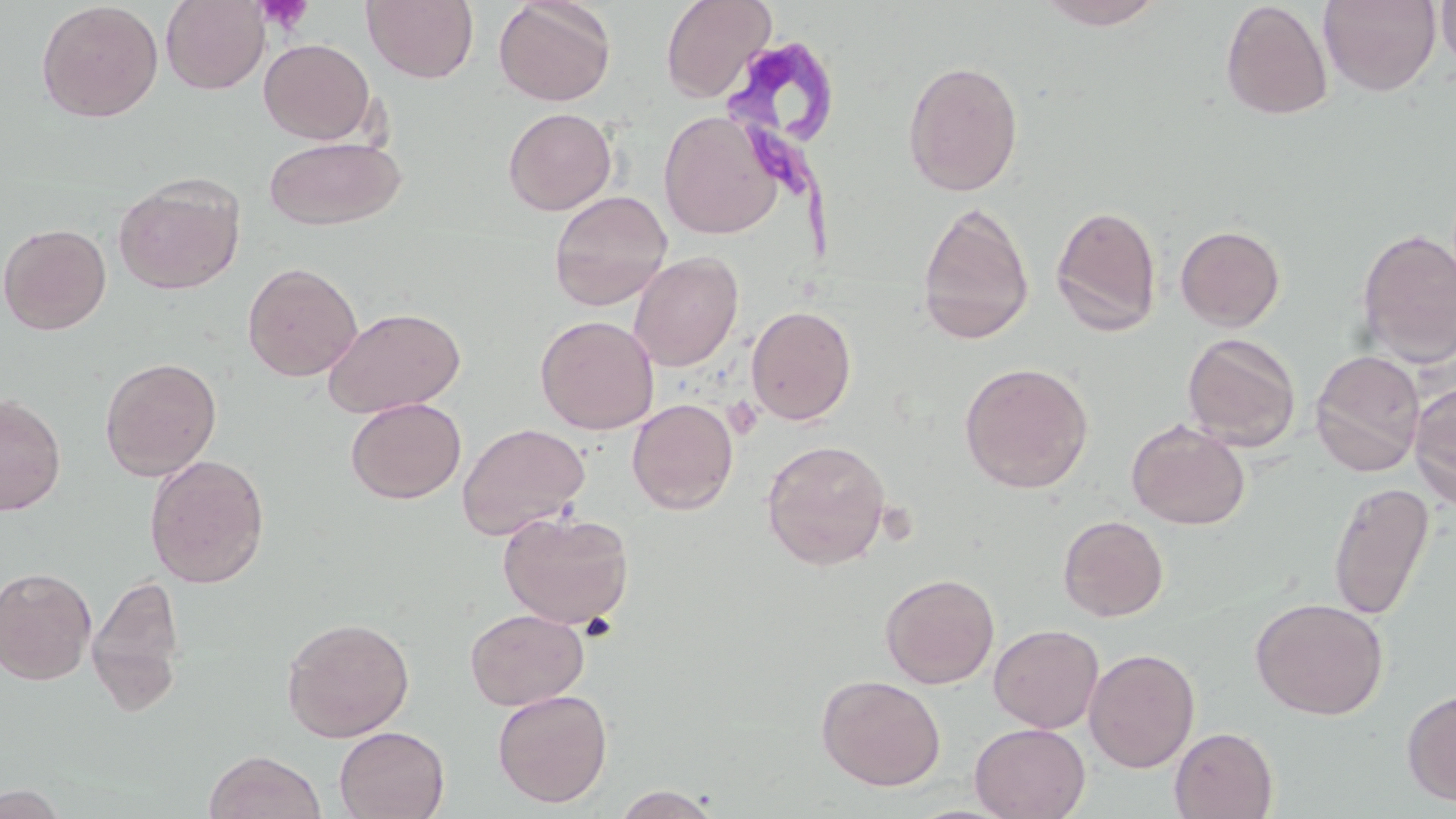
Summary:
  - Coordinate format: approximate bounding boxes as [x1, y1, x2, y2] in pixels
  - Trypanosoma brucei locations: [724, 47, 861, 261]
  - Uninfected red blood cell locations: [362, 0, 479, 84], [493, 0, 616, 107], [660, 0, 776, 103], [1035, 0, 1168, 30], [36, 1, 163, 123], [161, 1, 270, 94], [1219, 1, 1333, 120], [1318, 1, 1442, 96], [1435, 1, 1456, 76], [259, 38, 376, 144], [902, 59, 1024, 197], [503, 107, 616, 215], [659, 110, 782, 239], [264, 136, 406, 231], [114, 175, 244, 295], [549, 190, 672, 310], [917, 202, 1034, 345], [1050, 204, 1163, 336], [0, 222, 112, 335], [1175, 224, 1286, 331], [1355, 228, 1456, 367], [628, 251, 744, 371], [242, 262, 362, 382], [746, 305, 857, 425], [324, 307, 465, 418], [535, 315, 658, 434], [1182, 332, 1301, 452], [1309, 349, 1425, 477], [99, 356, 221, 481], [959, 362, 1094, 493], [1408, 380, 1456, 511], [0, 392, 67, 516], [345, 397, 467, 504], [627, 398, 738, 514], [1126, 420, 1250, 530], [457, 422, 590, 540], [761, 439, 891, 569], [144, 454, 270, 588], [1327, 480, 1435, 620], [497, 509, 635, 629], [1058, 515, 1169, 622], [0, 567, 97, 684], [87, 572, 187, 713], [880, 572, 1000, 688], [1250, 597, 1388, 720], [464, 608, 589, 711], [281, 616, 415, 742], [988, 624, 1104, 733], [1084, 647, 1200, 773], [816, 674, 945, 791], [1401, 687, 1456, 808], [492, 688, 612, 808], [970, 722, 1090, 819], [334, 726, 450, 819], [1170, 727, 1278, 819], [204, 749, 326, 819], [0, 785, 70, 819], [608, 785, 725, 818]
  - Platelet locations: [255, 0, 314, 36], [724, 397, 763, 439]
  - Slide-level diagnosis: Trypanosoma brucei
  - Stain: May-Grünwald-Giemsa
  - Image size: 1456×819 pixels
  - Modality: light microscopy
  - Field of view: one of a larger specimen
  - Preparation: thin blood smear
  - Magnification: 1000x